Describe the morphology of the red blood cells.
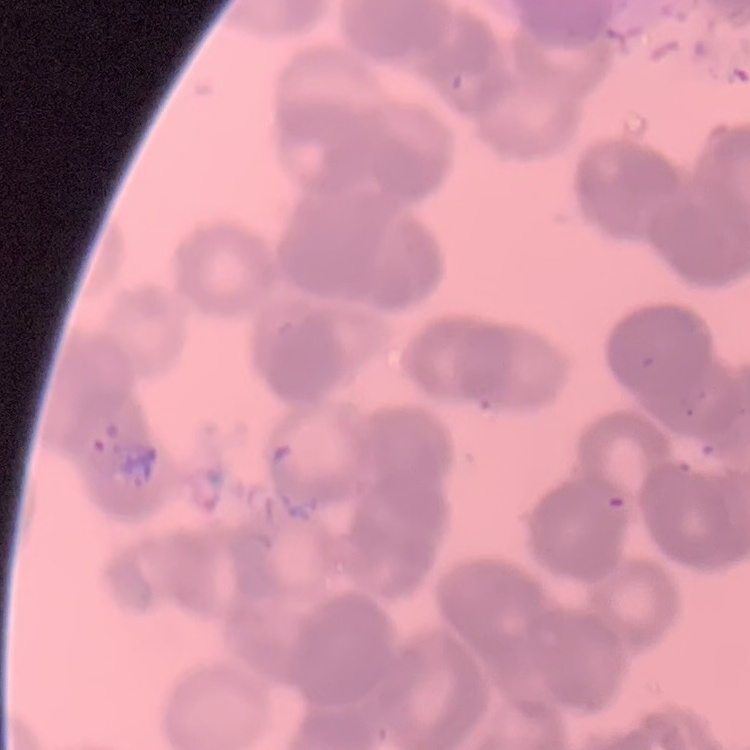
They show rouleaux formation.

Summary:
  - Preparation: thin blood smear
  - Stain: Field's or Giemsa
  - Image type: square crop of a larger photomicrograph